Look for Plasmodium parasites.
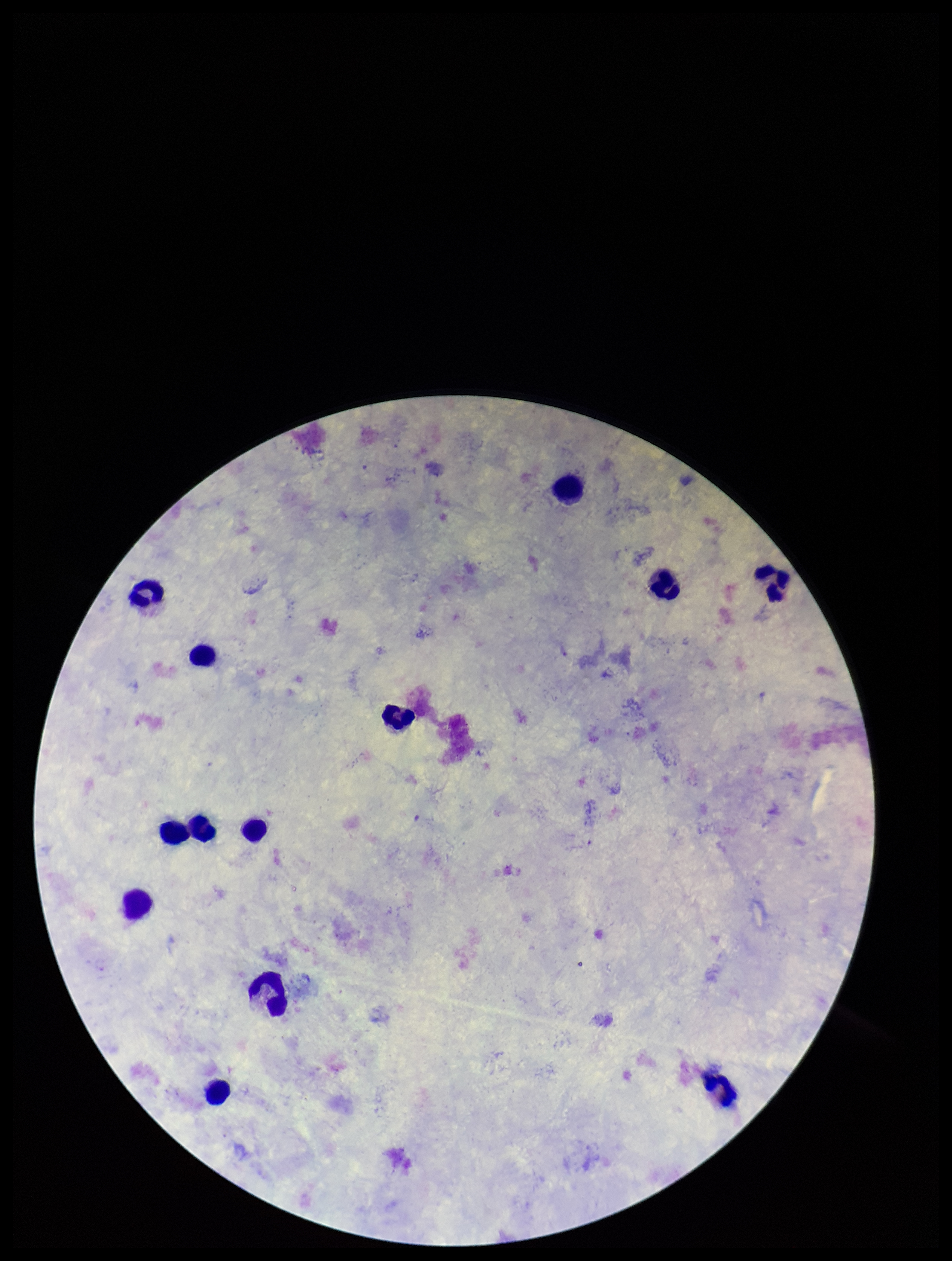

None detected.

Parasite count: 0. Preparation: thick blood smear. Photographed through the microscope eyepiece with a smartphone camera. Patient malaria status: negative. Leukocyte count: 13. Image is 952×1261 pixels. Giemsa stain. One field from this slide.